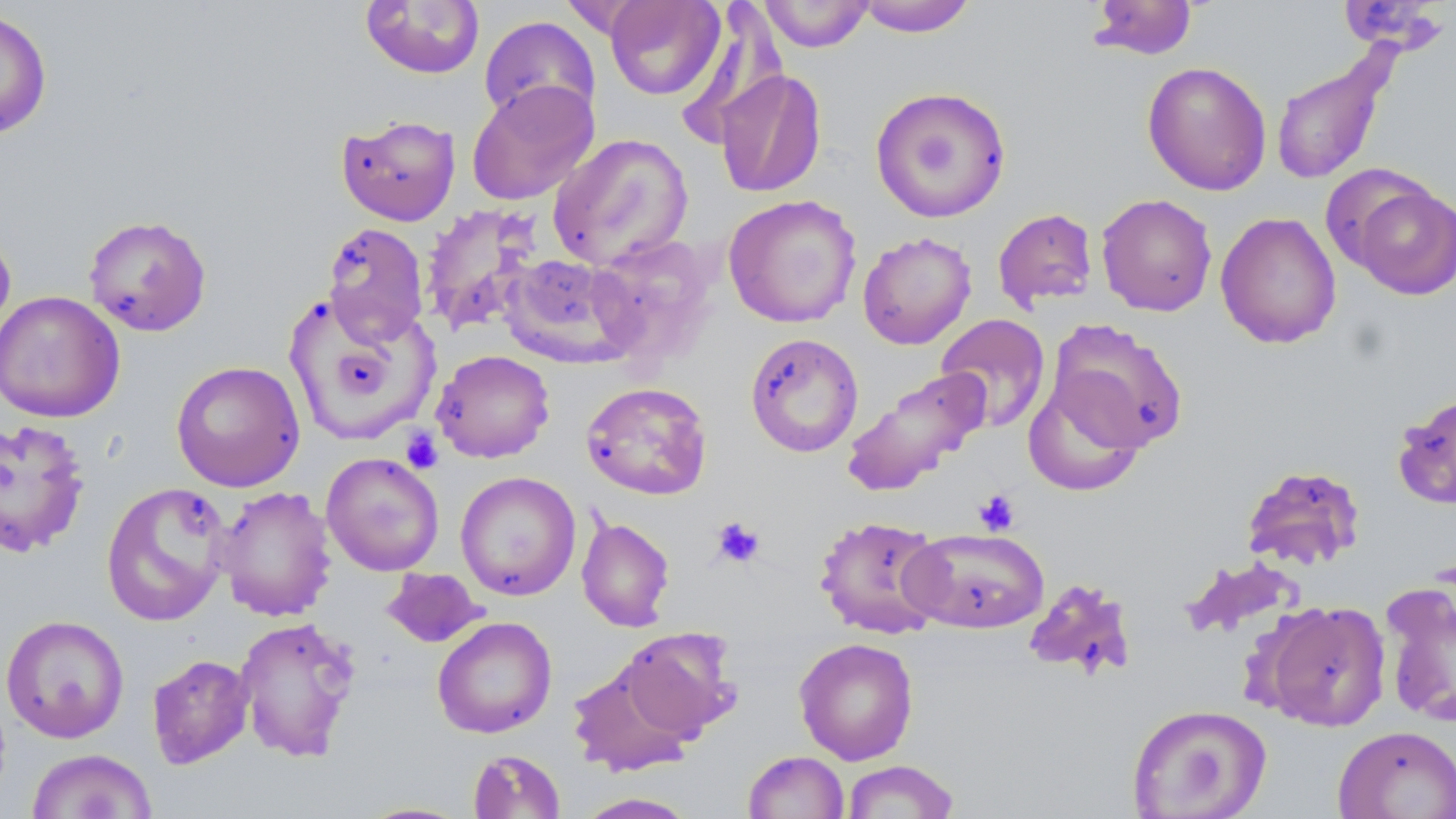
Summary:
  - Coordinate format: approximate bounding boxes as named x1/y1/x2/y2 corners in pixels
  - Platelet locations: (x1=401, y1=429, x2=443, y2=473), (x1=974, y1=489, x2=1020, y2=536), (x1=711, y1=517, x2=765, y2=568)
  - Uninfected red blood cell locations: (x1=603, y1=0, x2=726, y2=100), (x1=758, y1=0, x2=874, y2=52), (x1=857, y1=0, x2=976, y2=36), (x1=359, y1=1, x2=485, y2=79), (x1=1087, y1=1, x2=1199, y2=61), (x1=1336, y1=1, x2=1452, y2=56), (x1=0, y1=8, x2=53, y2=139), (x1=479, y1=15, x2=601, y2=127), (x1=1269, y1=51, x2=1395, y2=187), (x1=1142, y1=61, x2=1272, y2=196), (x1=715, y1=68, x2=827, y2=199), (x1=466, y1=80, x2=600, y2=206), (x1=869, y1=85, x2=1013, y2=224), (x1=336, y1=114, x2=461, y2=226), (x1=548, y1=133, x2=694, y2=271), (x1=1345, y1=179, x2=1456, y2=300), (x1=723, y1=194, x2=862, y2=328), (x1=1096, y1=194, x2=1217, y2=317), (x1=419, y1=203, x2=542, y2=335), (x1=992, y1=207, x2=1098, y2=311), (x1=1215, y1=212, x2=1342, y2=349), (x1=83, y1=214, x2=212, y2=337), (x1=322, y1=222, x2=430, y2=345), (x1=0, y1=225, x2=16, y2=347), (x1=857, y1=231, x2=977, y2=350), (x1=586, y1=233, x2=719, y2=364), (x1=499, y1=254, x2=636, y2=366), (x1=0, y1=290, x2=125, y2=423), (x1=282, y1=291, x2=440, y2=447), (x1=935, y1=313, x2=1051, y2=432), (x1=1046, y1=318, x2=1188, y2=453), (x1=745, y1=332, x2=864, y2=458), (x1=432, y1=349, x2=555, y2=463), (x1=170, y1=360, x2=306, y2=492), (x1=841, y1=366, x2=991, y2=496), (x1=1023, y1=375, x2=1147, y2=496), (x1=581, y1=382, x2=712, y2=500), (x1=1391, y1=390, x2=1456, y2=511), (x1=0, y1=417, x2=91, y2=558), (x1=321, y1=452, x2=445, y2=577), (x1=1240, y1=464, x2=1366, y2=572), (x1=455, y1=471, x2=581, y2=601), (x1=100, y1=481, x2=233, y2=627), (x1=213, y1=485, x2=337, y2=622), (x1=814, y1=514, x2=947, y2=639), (x1=576, y1=516, x2=675, y2=632), (x1=905, y1=527, x2=1049, y2=634), (x1=1179, y1=556, x2=1305, y2=640), (x1=382, y1=568, x2=486, y2=648), (x1=1022, y1=578, x2=1139, y2=681), (x1=1381, y1=580, x2=1456, y2=730), (x1=1262, y1=600, x2=1392, y2=731), (x1=1, y1=614, x2=130, y2=743), (x1=234, y1=615, x2=361, y2=763), (x1=432, y1=615, x2=557, y2=739), (x1=618, y1=629, x2=740, y2=743), (x1=793, y1=637, x2=919, y2=765), (x1=147, y1=654, x2=254, y2=769), (x1=568, y1=659, x2=699, y2=776), (x1=1126, y1=703, x2=1272, y2=818), (x1=1333, y1=725, x2=1456, y2=819), (x1=25, y1=749, x2=157, y2=818), (x1=467, y1=749, x2=566, y2=818), (x1=743, y1=751, x2=850, y2=818), (x1=841, y1=759, x2=960, y2=818), (x1=575, y1=792, x2=699, y2=818), (x1=354, y1=801, x2=474, y2=818)
  - Slide-level diagnosis: negative for blood parasites
  - Modality: light microscopy
  - Preparation: thin blood film
  - Image size: 1456×819 pixels
  - Stain: May-Grünwald-Giemsa
  - Magnification: 1000x
  - Field of view: single